Name the parasite shown.
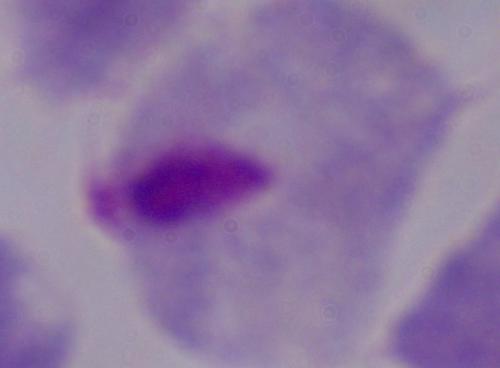

This is a trichomonad.

modality: micrograph
magnification: 1000x